Outline each blood parasite and name the species.
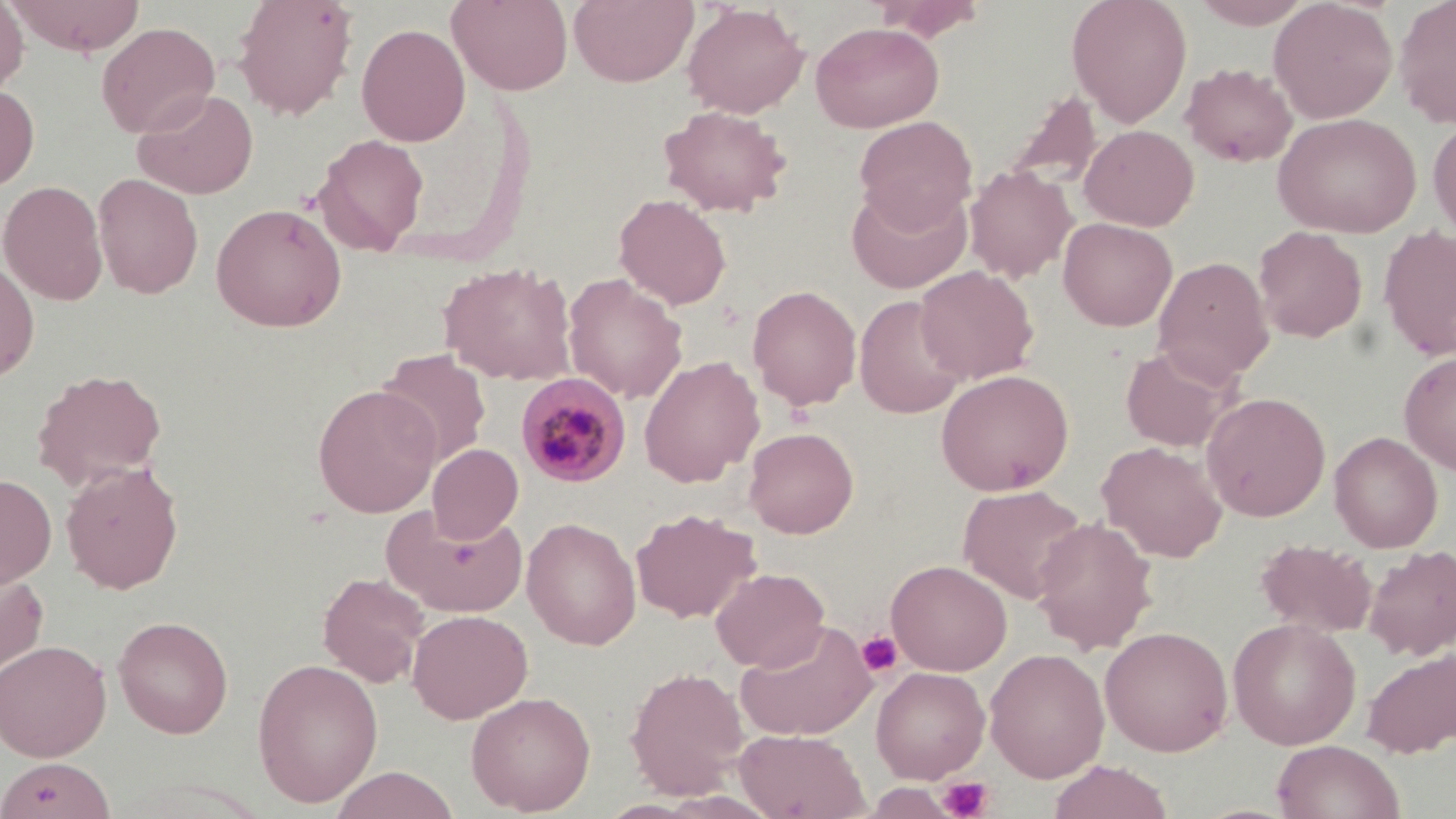

Approximate bounding boxes as (x1, y1, x2, y2) in pixels.
Plasmodium malariae-infected red blood cells: (515, 371, 631, 487).
No Plasmodium falciparum, Plasmodium ovale, Plasmodium vivax, Babesia divergens, or Trypanosoma brucei observed.

Platelet locations: (857, 631, 901, 677), (938, 777, 993, 819). Uninfected red blood cell locations: (0, 0, 28, 98), (6, 0, 147, 56), (232, 0, 359, 120), (448, 0, 573, 95), (569, 0, 698, 87), (870, 0, 988, 41), (1066, 0, 1192, 128), (1189, 0, 1316, 28), (1269, 0, 1397, 123), (1393, 0, 1456, 128), (682, 3, 809, 118), (810, 21, 944, 133), (96, 22, 219, 138), (356, 23, 471, 146), (1181, 62, 1298, 167), (0, 83, 39, 191), (133, 87, 259, 199), (1005, 89, 1101, 190), (658, 105, 792, 216), (1273, 113, 1421, 237), (854, 115, 977, 229), (1428, 115, 1456, 243), (1080, 124, 1198, 231), (313, 134, 429, 255), (964, 165, 1077, 282), (93, 173, 203, 299), (1, 179, 108, 306), (846, 182, 972, 294), (613, 193, 732, 310), (210, 202, 347, 332), (1058, 217, 1178, 331), (1253, 226, 1367, 342), (1378, 227, 1456, 361), (1153, 256, 1275, 385), (0, 259, 39, 383), (439, 260, 577, 386), (915, 265, 1039, 384), (562, 273, 688, 403), (747, 285, 862, 411), (854, 294, 968, 418), (1120, 344, 1239, 452), (377, 348, 493, 469), (1399, 351, 1456, 474), (639, 355, 764, 487), (31, 369, 168, 489), (935, 369, 1074, 496), (312, 384, 442, 517), (1201, 391, 1331, 521), (744, 426, 859, 538), (1330, 431, 1443, 552), (1097, 441, 1228, 562), (428, 443, 522, 543), (61, 461, 184, 594), (0, 474, 57, 588), (959, 484, 1088, 603), (382, 503, 527, 617), (630, 507, 759, 623), (1031, 516, 1158, 654), (521, 517, 641, 650), (1256, 539, 1377, 638), (1363, 544, 1456, 661), (886, 559, 1012, 676), (0, 564, 49, 680), (711, 567, 830, 672), (317, 572, 430, 688), (407, 609, 532, 723), (113, 616, 233, 738), (1227, 617, 1361, 749), (735, 620, 878, 741), (1099, 625, 1234, 756), (0, 639, 112, 762), (1361, 647, 1456, 758), (985, 648, 1110, 782), (251, 657, 383, 807), (625, 666, 749, 799), (871, 666, 990, 783), (466, 690, 596, 815), (735, 729, 869, 819), (1272, 739, 1404, 819), (2, 758, 113, 817), (1048, 760, 1173, 819), (329, 766, 460, 819). Slide-level diagnosis: Plasmodium malariae. May-Grünwald-Giemsa-stained preparation. Light microscopy. 1000x magnification. One field of a larger specimen. Image is 1456×819 pixels. Thin blood smear.